State which parasite is depicted.
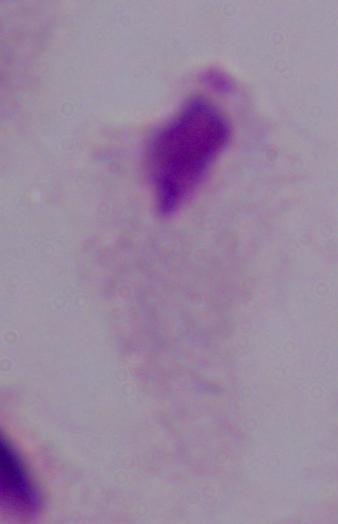

This is a trichomonad.

1000x magnification. Photomicrograph.